Name the cell type shown.
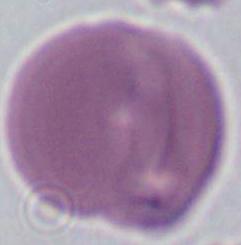

An erythrocyte.

Photomicrograph. 1000x magnification.